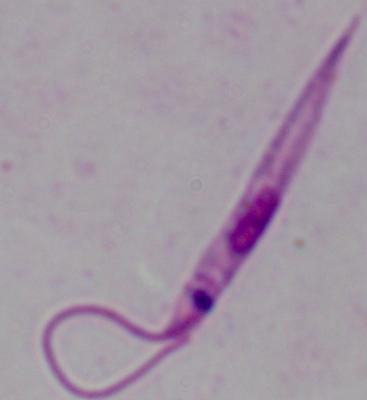
{
  "identification": "Leishmania",
  "magnification": "1000x",
  "modality": "micrograph"
}